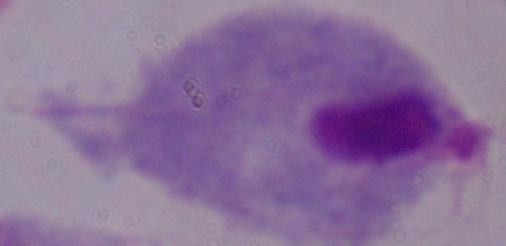
Summary:
  - Magnification: 1000x
  - Modality: photomicrograph
  - Identification: trichomonad